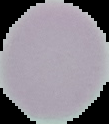

From a thin blood film. Image is 109×124 pixels. The area outside the segmented cell region is set to black. Malaria status: uninfected.